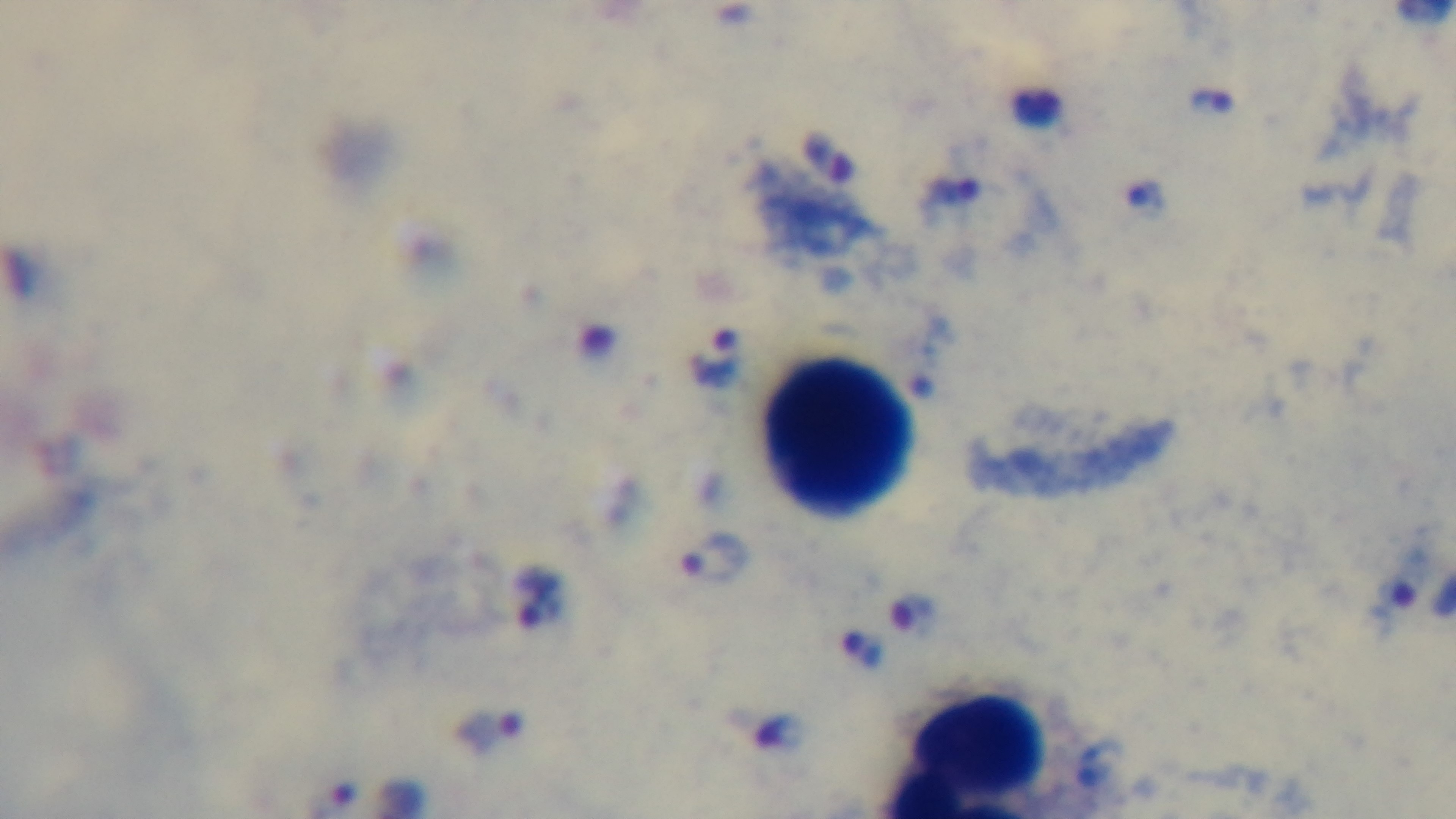
capture = mounted 4K digital camera
modality = light microscopy
preparation = thick
stain = Giemsa
objective = 100x oil immersion
field of view = single
malaria status = positive